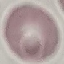
Result: no malaria parasites detected. Thin blood smear. Giemsa-stained preparation. Acquired by smartphone through the microscope eyepiece. Cell patch, automatically extracted from a larger field of view and resized to 64 × 64 pixels.